Locate every Plasmodium parasite.
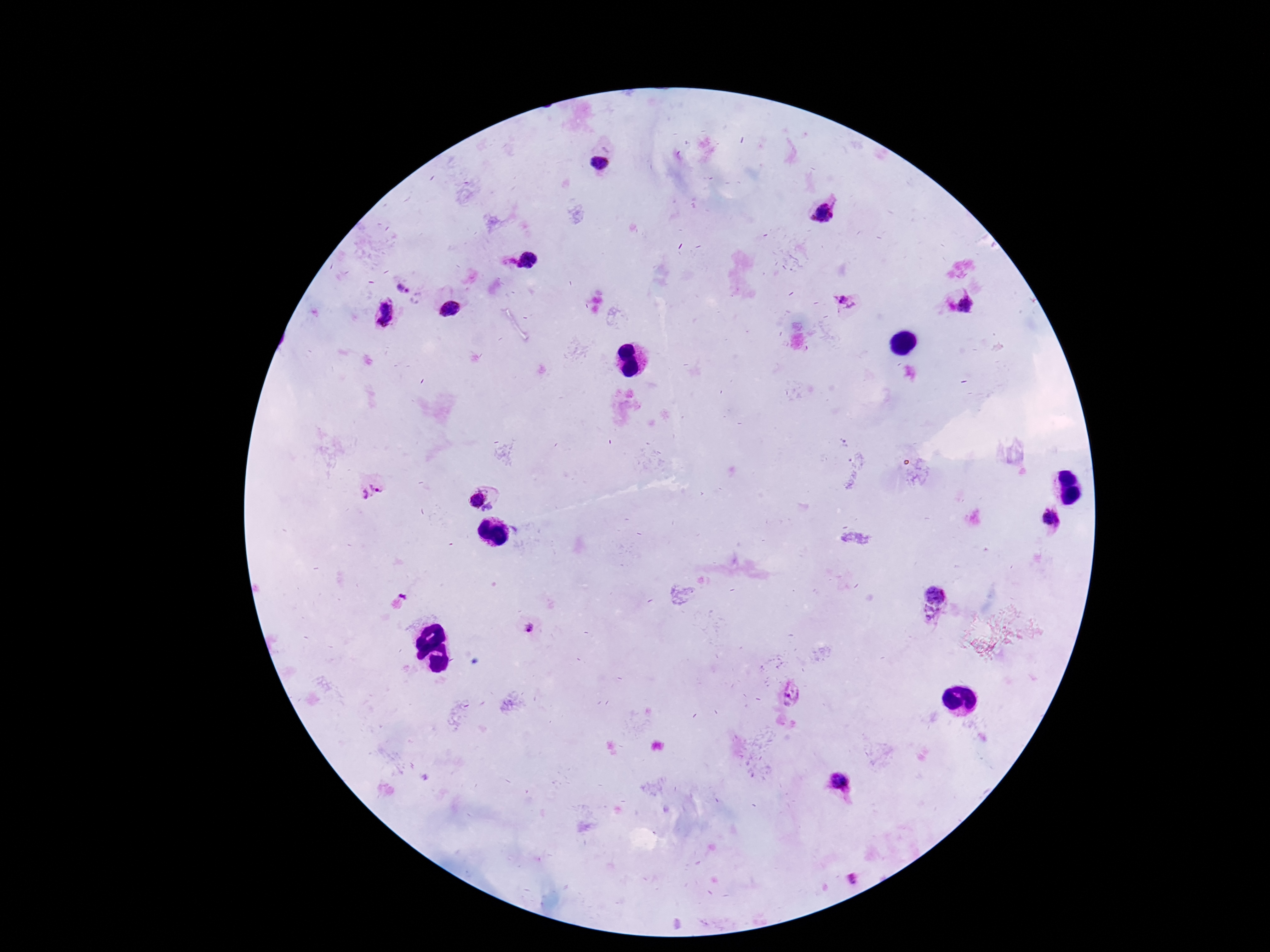
Approximate centers as [x, y] in pixels.
Plasmodium parasites: [598, 163], [824, 212], [528, 260], [403, 289], [847, 301], [967, 303], [450, 309], [383, 312], [371, 490], [473, 498], [488, 509], [1052, 519], [937, 595], [402, 600], [933, 617], [530, 626], [791, 694], [843, 782], [852, 880].

Giemsa-stained preparation. Patient malaria status: positive. Image is 1270×952 pixels. Thick blood film. Photographed through the microscope eyepiece with a smartphone camera. 100x magnification. Single field of view.